Locate every blood parasite and identify its species.
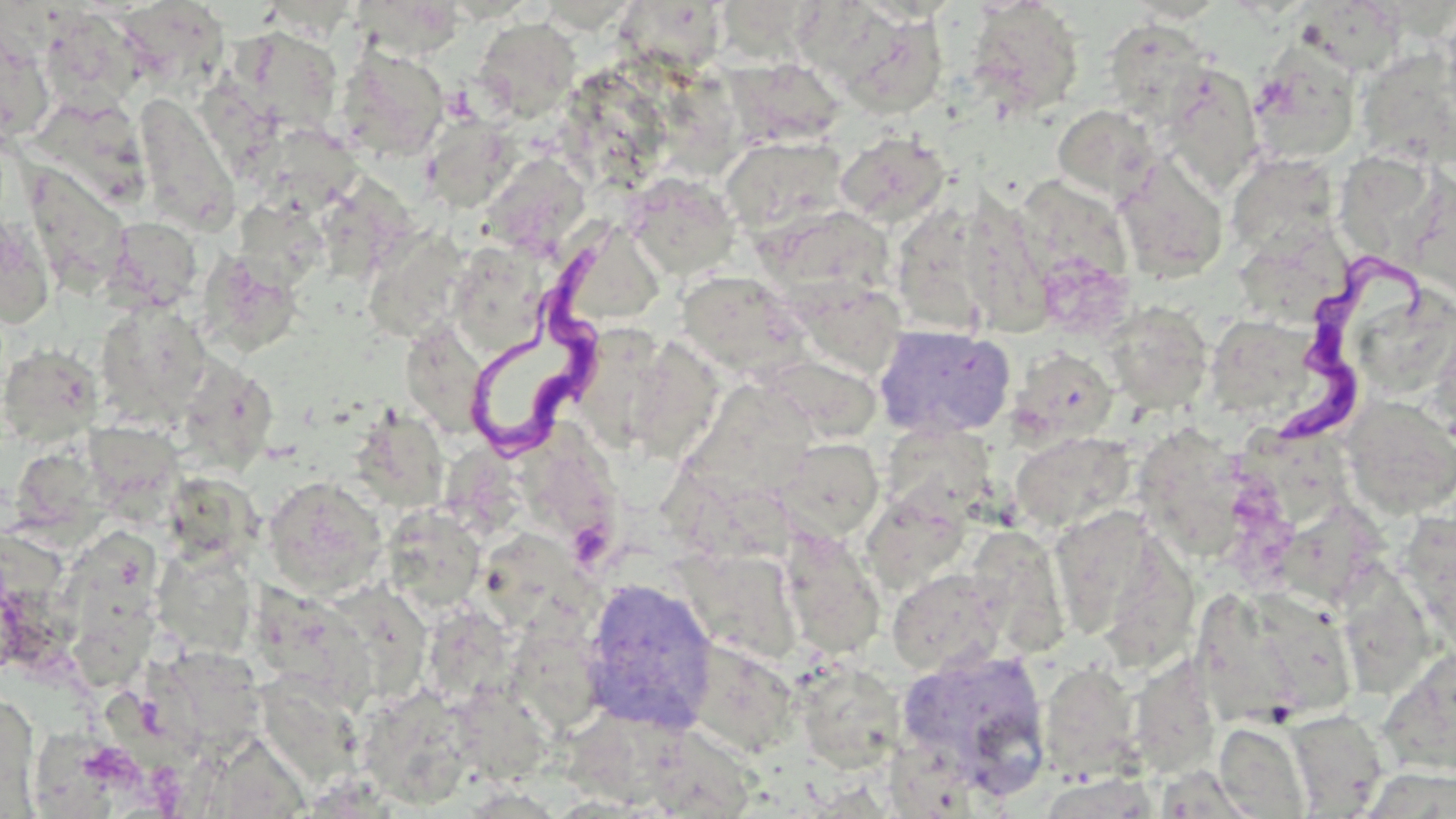

Approximate bounding boxes as (x1, y1, x2, y2) in pixels.
Trypanosoma brucei: (473, 237, 615, 454), (1278, 242, 1437, 450).
No Plasmodium falciparum, Plasmodium ovale, Plasmodium malariae, Plasmodium vivax, or Babesia divergens observed.

Uninfected red blood cell locations: (352, 0, 465, 61), (615, 2, 729, 76), (964, 2, 1086, 118), (1288, 3, 1400, 80), (725, 5, 826, 72), (819, 6, 950, 118), (130, 7, 248, 104), (39, 9, 146, 117), (474, 17, 581, 121), (0, 19, 56, 146), (1103, 19, 1215, 122), (235, 27, 345, 136), (336, 45, 449, 161), (1354, 45, 1455, 171), (1246, 50, 1361, 167), (727, 57, 846, 148), (1158, 64, 1263, 194), (677, 78, 745, 163), (206, 86, 291, 183), (134, 91, 240, 235), (1052, 104, 1160, 205), (422, 114, 515, 211), (271, 129, 365, 207), (835, 131, 951, 228), (720, 134, 849, 236), (1225, 152, 1340, 257), (479, 153, 593, 253), (1114, 154, 1229, 284), (1350, 161, 1429, 249), (24, 164, 131, 295), (624, 172, 740, 282), (327, 175, 420, 277), (1013, 176, 1132, 293), (954, 189, 1057, 337), (234, 197, 328, 289), (761, 204, 896, 306), (0, 215, 56, 328), (104, 218, 204, 313), (362, 227, 471, 344), (447, 242, 551, 358), (1243, 242, 1353, 328), (199, 250, 304, 357), (1037, 255, 1136, 341), (675, 270, 810, 378), (790, 275, 918, 368), (95, 301, 211, 425), (1101, 302, 1213, 413), (879, 323, 1021, 439), (1219, 324, 1317, 414), (584, 332, 654, 462), (749, 338, 887, 456), (1, 344, 104, 447), (408, 345, 493, 432), (642, 346, 717, 469), (1013, 349, 1117, 446), (174, 356, 278, 474), (715, 385, 826, 481), (1341, 396, 1456, 519), (363, 415, 452, 507), (1137, 420, 1255, 578), (87, 421, 197, 519), (1009, 431, 1135, 533), (532, 436, 633, 553), (777, 437, 884, 540), (1260, 439, 1358, 528), (454, 446, 527, 528), (7, 452, 114, 550), (262, 476, 387, 597), (182, 483, 267, 573), (861, 491, 972, 594), (1046, 505, 1180, 645), (381, 506, 487, 612), (1400, 511, 1455, 655), (79, 521, 159, 684), (1295, 521, 1394, 611), (779, 529, 885, 661), (489, 538, 611, 633), (948, 539, 1065, 669), (153, 545, 257, 659), (676, 549, 803, 666), (887, 567, 1010, 677), (1339, 570, 1421, 700), (581, 576, 719, 732), (332, 577, 426, 698), (259, 588, 383, 715), (1200, 596, 1295, 733), (1256, 596, 1354, 715), (436, 615, 517, 707), (504, 623, 609, 737), (685, 640, 800, 756), (893, 646, 1052, 792), (1378, 646, 1456, 776), (168, 647, 269, 750), (1126, 654, 1221, 779), (794, 660, 906, 771), (1039, 661, 1142, 781), (271, 678, 375, 782), (1, 690, 40, 815), (377, 691, 477, 810), (472, 704, 546, 784), (1286, 710, 1389, 816), (563, 712, 674, 805), (1214, 722, 1311, 817), (638, 726, 740, 818), (214, 727, 302, 812), (1033, 772, 1162, 818). Slide-level diagnosis: Trypanosoma brucei. Thin blood film. Optical microscopy. Image is 1456×819 pixels. One field of a larger specimen. Captured at 1000x magnification. May-Grünwald-Giemsa stain.